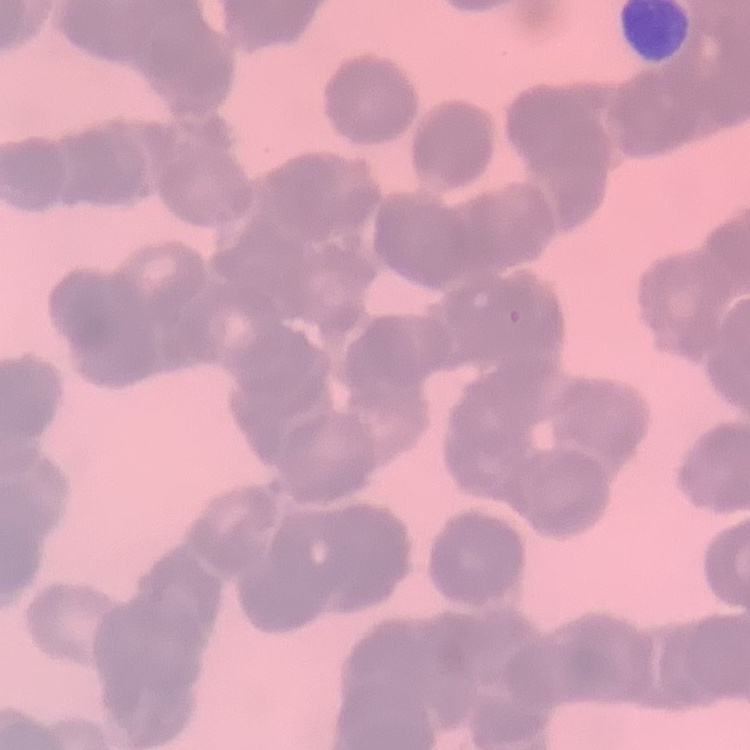

red blood cell morphology = rouleaux formation
preparation = thin peripheral smear
image type = one tile cut from a larger photomicrograph
stain = Field's or Giemsa